State which parasite is depicted.
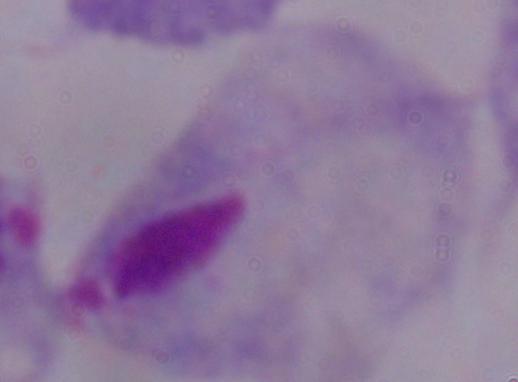

This is a trichomonad.

Captured at 1000x magnification. Photomicrograph.